Comment on the morphology of the red blood cells.
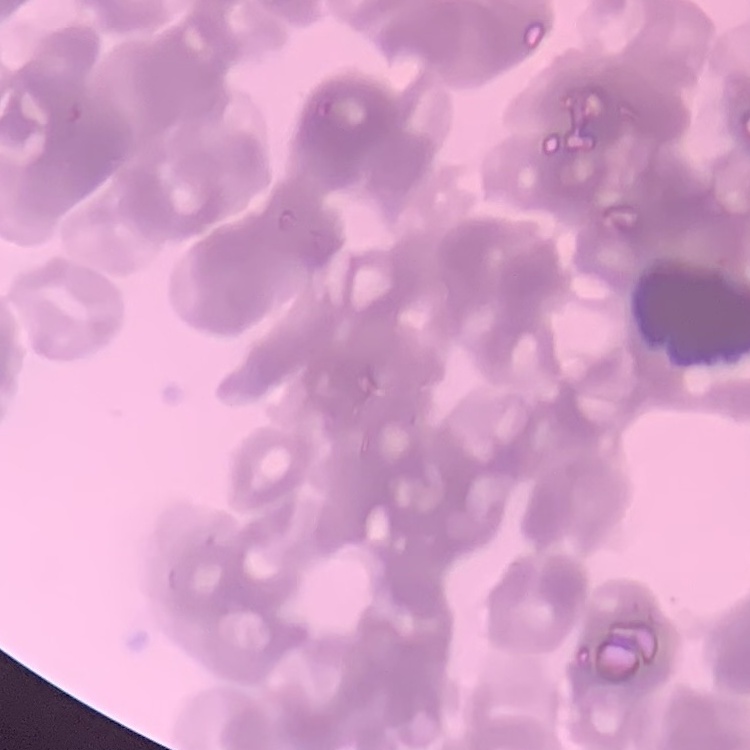

Rouleaux formation.

Summary:
  - Preparation: thin peripheral smear
  - Image type: square crop of a larger photomicrograph
  - Stain: Field's or Giemsa